Outline each blood parasite and name the species.
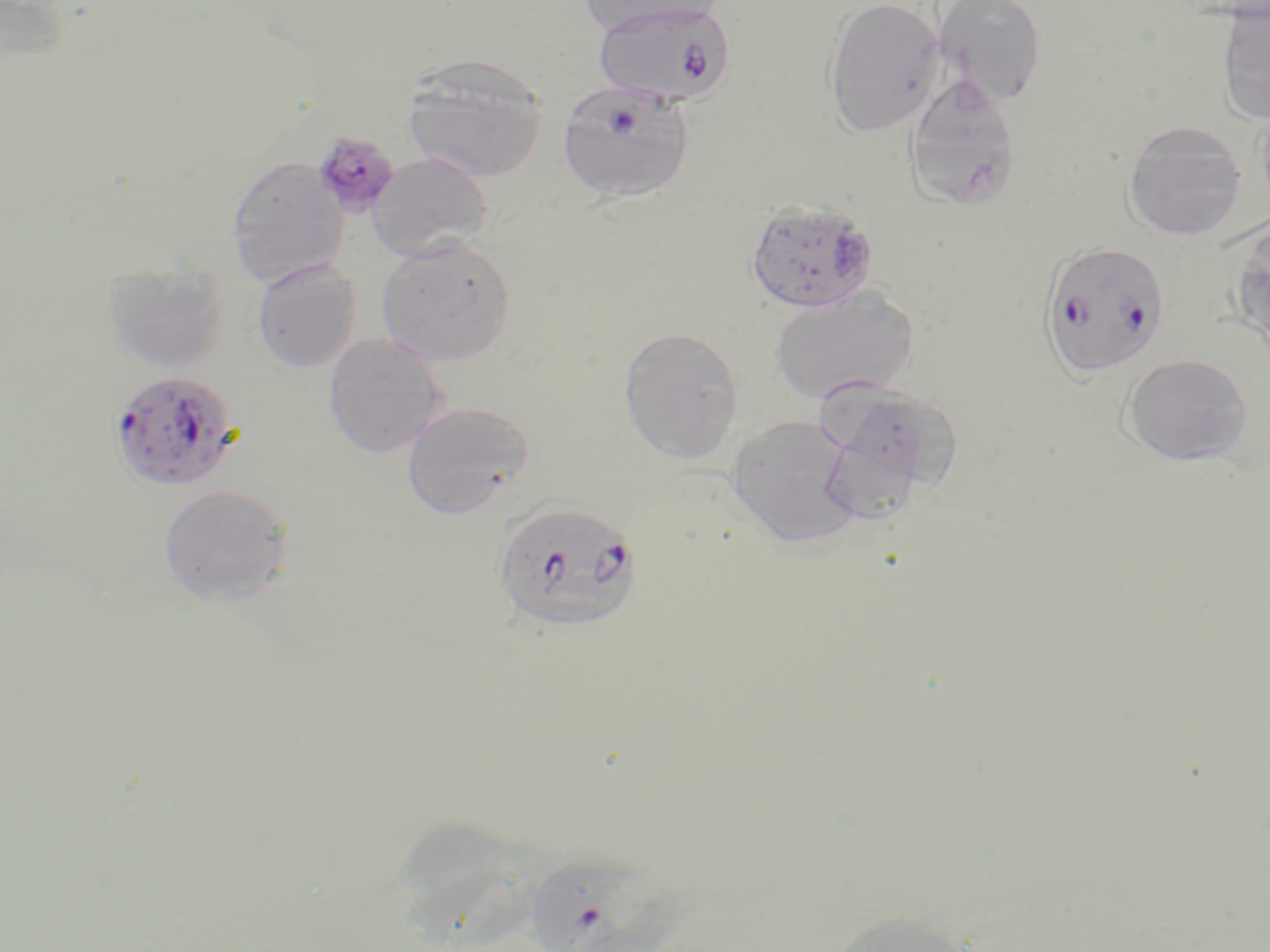
Approximate bounding boxes as (x1,y1)-(x2,y2) corner pairs in pixels.
Plasmodium falciparum-infected red blood cells: (592,2)-(737,107), (556,79)-(696,203), (745,200)-(880,314), (1039,240)-(1170,380), (108,369)-(240,492), (491,499)-(644,635), (525,860)-(709,952).
No Plasmodium ovale, Plasmodium malariae, Plasmodium vivax, Babesia divergens, or Trypanosoma brucei observed.

Summary:
  - Platelet locations: (304,128)-(399,223)
  - Uninfected red blood cell locations: (577,0)-(724,38), (822,0)-(945,138), (931,0)-(1048,105), (1215,3)-(1270,125), (402,53)-(550,184), (904,72)-(1023,211), (1121,120)-(1247,242), (368,152)-(493,261), (227,156)-(348,289), (1228,219)-(1270,351), (376,236)-(517,366), (251,258)-(361,374), (104,262)-(229,375), (769,285)-(920,406), (618,325)-(744,464), (323,332)-(449,458), (1119,354)-(1255,466), (814,385)-(951,522), (401,401)-(535,520), (726,414)-(863,549), (159,484)-(295,606), (402,820)-(545,952), (828,909)-(977,952)
  - Slide-level diagnosis: Plasmodium falciparum
  - Stain: May-Grünwald-Giemsa
  - Magnification: 1000x
  - Modality: light microscopy
  - Image size: 1270×952 pixels
  - Preparation: thin blood film
  - Field of view: one of a larger specimen